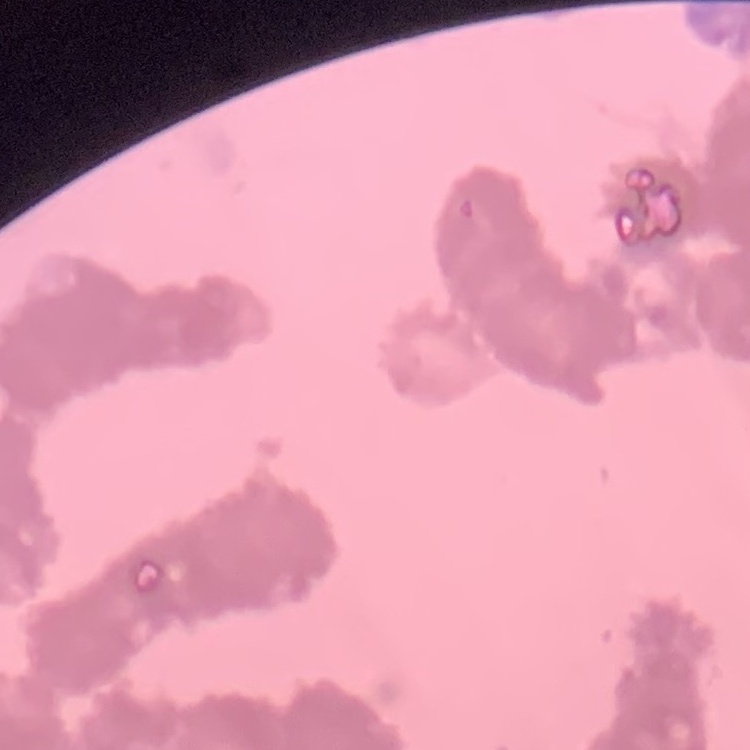

Summary:
  - Erythrocyte morphology: rouleaux formation
  - Preparation: thin blood smear
  - Stain: Field's or Giemsa
  - Image type: square crop of a larger photomicrograph